Classify this cell by malaria status.
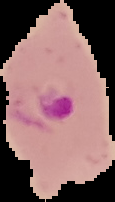

Parasitized.

{
  "image_type": "segmented cell region on a black background",
  "image_size": "115×202 pixels",
  "preparation": "thin blood film"
}